Locate every leukocyte (white blood cell).
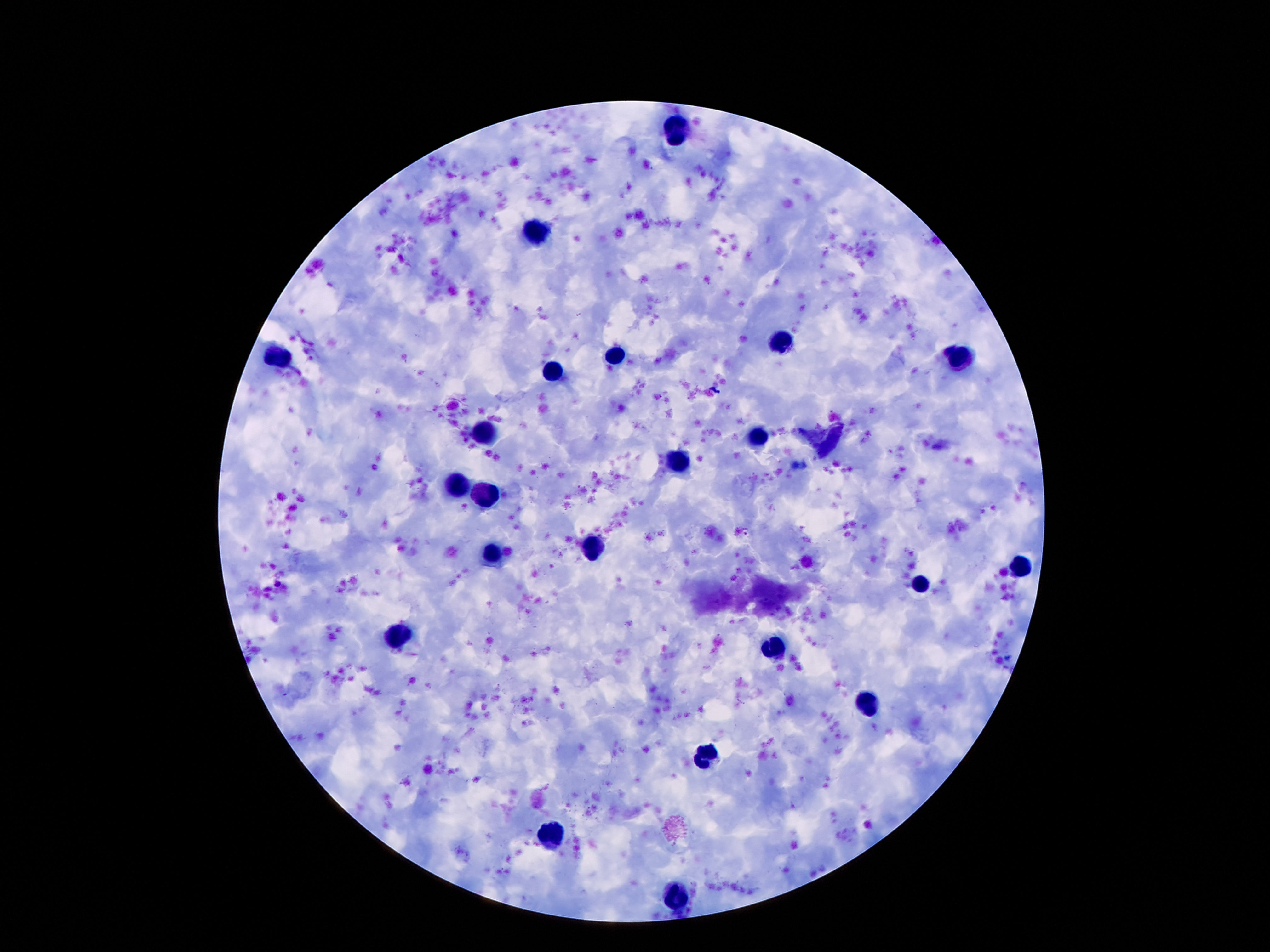

Approximate object centers, in pixels from the top-left corner.
Leukocytes: (x=679, y=129), (x=538, y=232), (x=784, y=343), (x=612, y=354), (x=281, y=355), (x=960, y=355), (x=554, y=371), (x=484, y=433), (x=758, y=436), (x=677, y=463), (x=459, y=487), (x=487, y=495), (x=595, y=548), (x=495, y=555), (x=1021, y=568), (x=920, y=581), (x=398, y=636), (x=774, y=647), (x=866, y=707), (x=706, y=758), (x=554, y=832), (x=677, y=896).

Summary:
  - Stain: Giemsa
  - Capture: smartphone camera through the microscope eyepiece
  - Image size: 1270×952 pixels
  - Preparation: thick blood film
  - Patient malaria status: negative
  - Magnification: 100x
  - Field of view: single